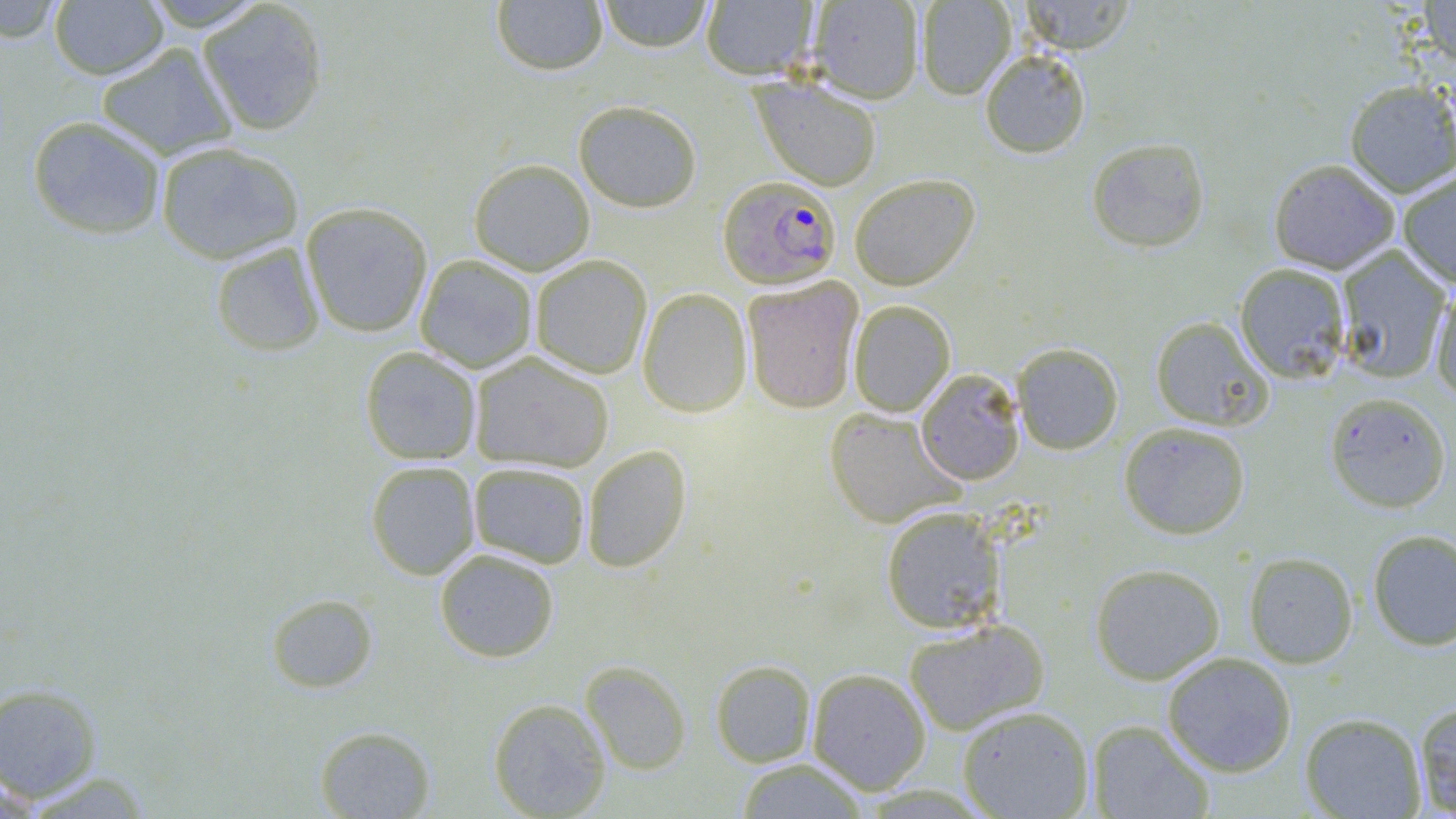
Summary:
  - Coordinate format: approximate bounding boxes as (x1, y1, x2, y2) in pixels
  - Plasmodium falciparum-infected red blood cell locations: (718, 175, 841, 288)
  - Uninfected red blood cell locations: (48, 0, 169, 80), (139, 0, 269, 31), (491, 0, 609, 76), (598, 0, 713, 52), (807, 0, 925, 104), (916, 0, 1017, 100), (1018, 0, 1138, 54), (1419, 0, 1456, 70), (0, 1, 66, 42), (197, 1, 329, 136), (700, 1, 818, 80), (96, 43, 237, 160), (979, 49, 1092, 158), (751, 76, 883, 190), (1344, 80, 1456, 198), (573, 99, 703, 212), (26, 115, 167, 239), (1086, 138, 1210, 252), (154, 141, 304, 264), (469, 158, 595, 275), (1268, 158, 1400, 274), (1397, 171, 1456, 288), (849, 173, 980, 291), (301, 201, 434, 338), (210, 242, 325, 356), (1335, 247, 1453, 383), (414, 254, 538, 373), (530, 255, 652, 379), (1234, 262, 1352, 383), (742, 277, 863, 413), (1429, 281, 1456, 405), (637, 287, 752, 418), (849, 299, 956, 416), (1150, 316, 1273, 431), (1012, 342, 1124, 454), (360, 346, 482, 465), (469, 351, 614, 473), (915, 368, 1025, 485), (1325, 391, 1451, 512), (823, 407, 965, 529), (1119, 421, 1251, 539), (581, 444, 692, 573), (366, 461, 480, 580), (468, 461, 591, 568), (880, 506, 1007, 634), (1367, 529, 1456, 651), (434, 548, 559, 662), (1243, 551, 1358, 669), (1089, 562, 1225, 685), (266, 593, 379, 693), (903, 618, 1050, 735), (1161, 652, 1297, 776), (711, 659, 816, 767), (580, 661, 692, 774), (807, 668, 931, 795), (0, 683, 102, 802), (488, 698, 612, 818), (1413, 700, 1456, 816), (957, 705, 1094, 818), (1300, 712, 1427, 818), (1087, 720, 1214, 818), (314, 725, 436, 818), (734, 758, 870, 818)
  - Slide-level diagnosis: Plasmodium falciparum
  - Modality: light microscopy
  - Image size: 1456×819 pixels
  - Field of view: single
  - Preparation: thin blood smear
  - Stain: May-Grünwald-Giemsa
  - Magnification: 1000x